Report the malaria status of this cell.
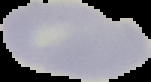

It is uninfected.

Summary:
  - Image size: 151×82 pixels
  - Preparation: thin blood film
  - Image type: cell region segmented out of the field of view; surrounding area masked to black